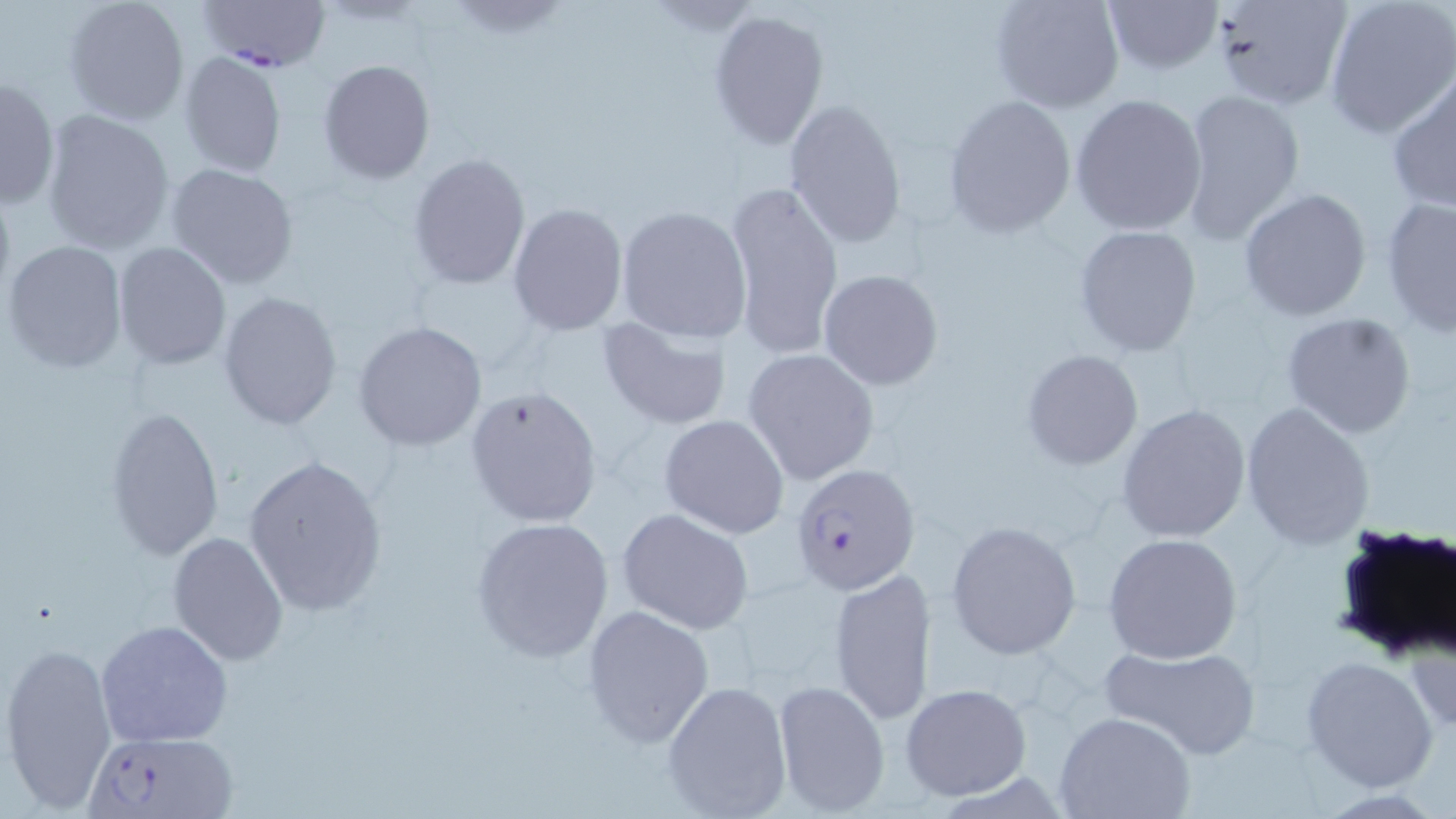
Summary:
  - Coordinate format: approximate bounding boxes as [x1, y1, x2, y2] in pixels
  - Uninfected red blood cell locations: [63, 0, 191, 127], [987, 0, 1126, 114], [1100, 0, 1222, 73], [1207, 0, 1351, 113], [1322, 0, 1456, 139], [707, 9, 829, 151], [179, 51, 288, 177], [319, 59, 435, 183], [1387, 72, 1456, 212], [1, 76, 60, 210], [1176, 87, 1307, 244], [1070, 93, 1207, 236], [942, 95, 1076, 236], [783, 98, 907, 249], [39, 109, 176, 255], [407, 152, 531, 292], [165, 162, 299, 289], [724, 180, 844, 359], [1239, 189, 1372, 323], [1380, 196, 1456, 340], [508, 202, 628, 335], [614, 205, 753, 345], [1073, 224, 1203, 356], [4, 240, 128, 373], [113, 242, 231, 370], [818, 270, 944, 390], [217, 291, 342, 431], [1280, 311, 1418, 439], [596, 315, 733, 429], [355, 320, 488, 452], [742, 347, 880, 484], [1021, 348, 1144, 471], [464, 386, 602, 527], [1118, 401, 1252, 543], [1239, 401, 1373, 550], [104, 405, 225, 560], [659, 414, 790, 540], [242, 452, 388, 618], [616, 509, 753, 634], [470, 517, 616, 663], [945, 521, 1082, 659], [167, 531, 289, 665], [1103, 532, 1243, 664], [830, 567, 935, 724], [580, 604, 716, 748], [96, 620, 233, 747], [3, 641, 118, 815], [1097, 643, 1262, 759], [1301, 655, 1439, 792], [660, 678, 794, 819], [771, 679, 890, 817], [901, 683, 1031, 800], [1053, 711, 1196, 819]
  - Plasmodium falciparum-infected red blood cell locations: [199, 0, 329, 73], [789, 462, 921, 596], [87, 731, 237, 819]
  - Slide-level diagnosis: Plasmodium falciparum
  - Image size: 1456×819 pixels
  - Modality: light microscopy
  - Preparation: thin blood smear
  - Magnification: 1000x
  - Field of view: one of a larger specimen
  - Stain: May-Grünwald-Giemsa